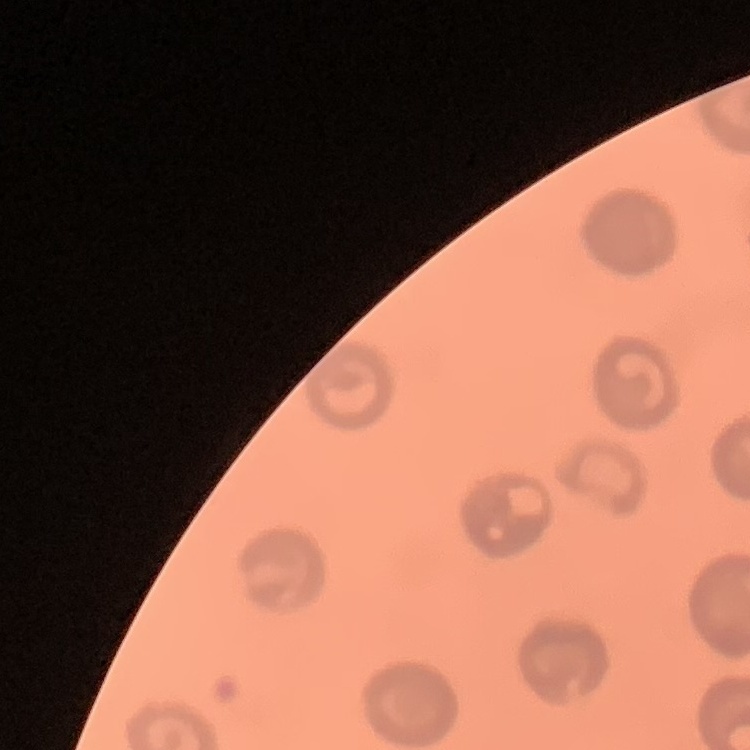 The red blood cells exhibit no rouleaux formation. Thin blood smear. One tile cut from a larger photomicrograph. Field's or Giemsa stain.